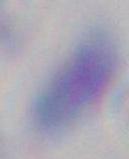

Summary:
  - Identification: Toxoplasma gondii
  - Modality: photomicrograph
  - Magnification: 1000x